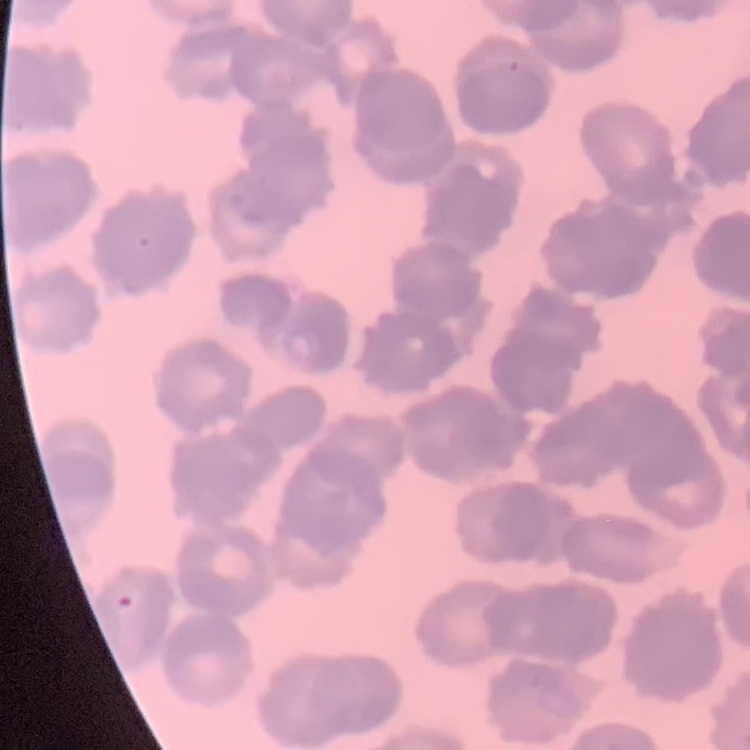

The red blood cells exhibit rouleaux formation. Stained with either Field's or Giemsa. One tile cut from a larger photomicrograph. Thin blood smear.